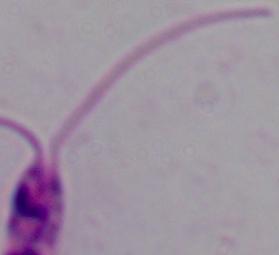
magnification = 1000x
modality = micrograph
identification = Leishmania